Give the extent of all Plasmodium malariae-infected red blood cells.
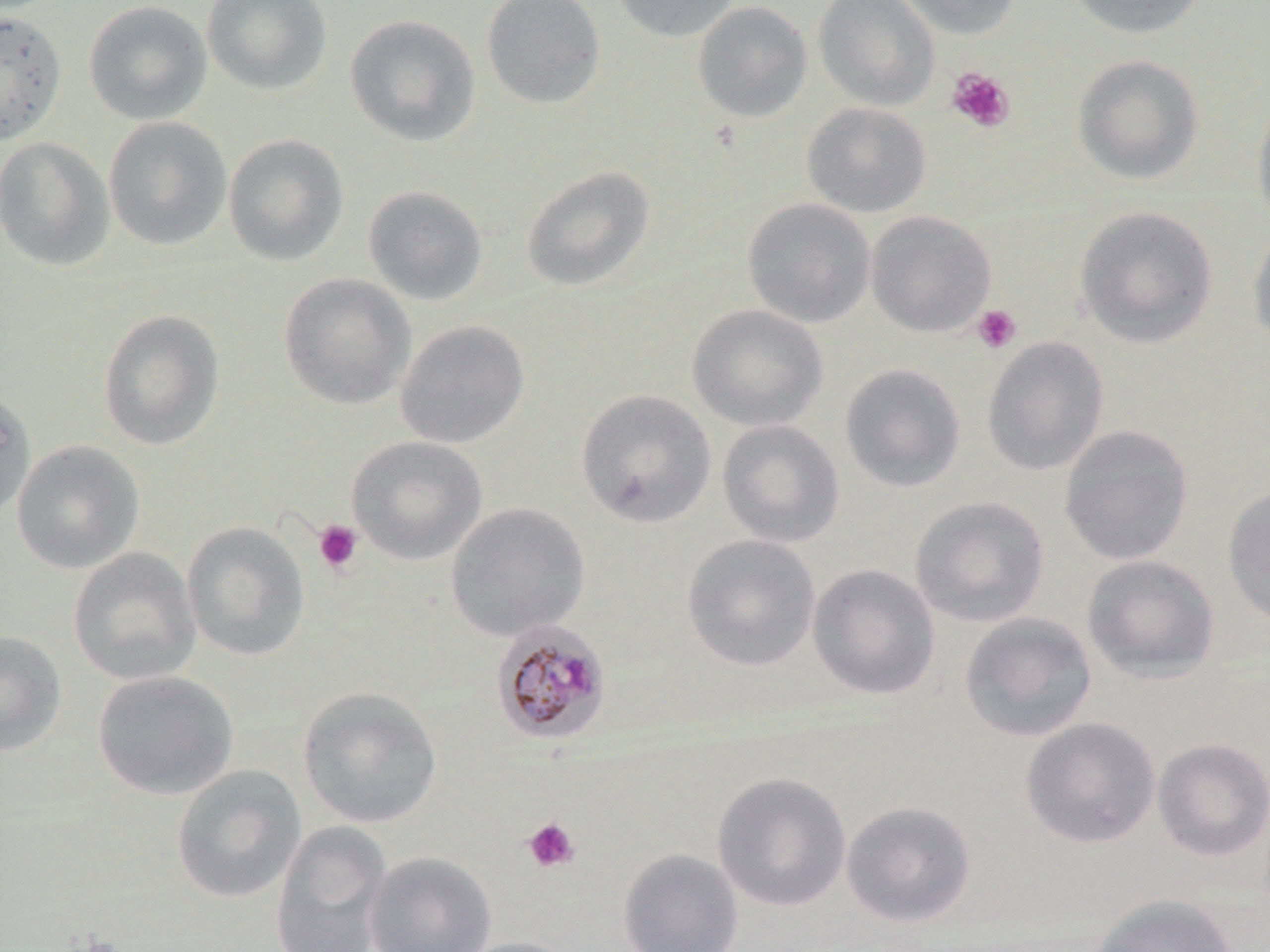
Approximate bounding boxes as (x1, y1, x2, y2) in pixels.
Plasmodium malariae-infected red blood cells: (490, 618, 612, 746).

Summary:
  - Uninfected red blood cell locations: (201, 0, 333, 96), (481, 0, 606, 109), (610, 0, 740, 42), (813, 0, 940, 111), (894, 0, 1023, 40), (1062, 0, 1210, 39), (83, 1, 213, 126), (692, 1, 813, 123), (0, 10, 68, 146), (344, 14, 481, 147), (1072, 54, 1205, 185), (1251, 95, 1270, 236), (801, 102, 932, 217), (103, 116, 233, 252), (223, 134, 349, 265), (0, 137, 115, 271), (521, 165, 656, 292), (363, 185, 489, 305), (742, 197, 876, 328), (1073, 205, 1218, 349), (866, 210, 997, 337), (1247, 226, 1270, 354), (278, 273, 416, 409), (687, 303, 829, 432), (97, 309, 225, 450), (394, 320, 530, 449), (981, 336, 1109, 477), (839, 363, 966, 493), (0, 388, 36, 524), (575, 389, 717, 529), (716, 419, 845, 549), (1058, 424, 1194, 566), (347, 436, 488, 565), (11, 440, 144, 574), (1221, 485, 1270, 626), (909, 495, 1050, 628), (445, 502, 591, 641), (182, 521, 311, 661), (681, 534, 821, 672), (68, 547, 201, 686), (1081, 554, 1221, 684), (807, 563, 941, 701), (958, 611, 1097, 743), (0, 630, 66, 757), (92, 670, 238, 799), (297, 685, 443, 829), (1020, 717, 1161, 849), (1152, 737, 1270, 862), (172, 765, 306, 903), (711, 772, 852, 912), (841, 800, 976, 928), (270, 820, 393, 952), (617, 848, 744, 952), (364, 851, 497, 952), (1088, 893, 1241, 952), (451, 936, 579, 952)
  - Platelet locations: (946, 67, 1015, 133), (971, 304, 1022, 354), (313, 519, 364, 575), (522, 817, 581, 873)
  - Slide-level diagnosis: Plasmodium malariae
  - Field of view: one of a larger specimen
  - Modality: optical microscopy
  - Stain: May-Grünwald-Giemsa
  - Image size: 1270×952 pixels
  - Magnification: 1000x
  - Preparation: thin blood film